State which parasite is depicted.
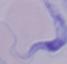

This is a trypanosome.

Summary:
  - Modality: micrograph
  - Magnification: 1000x